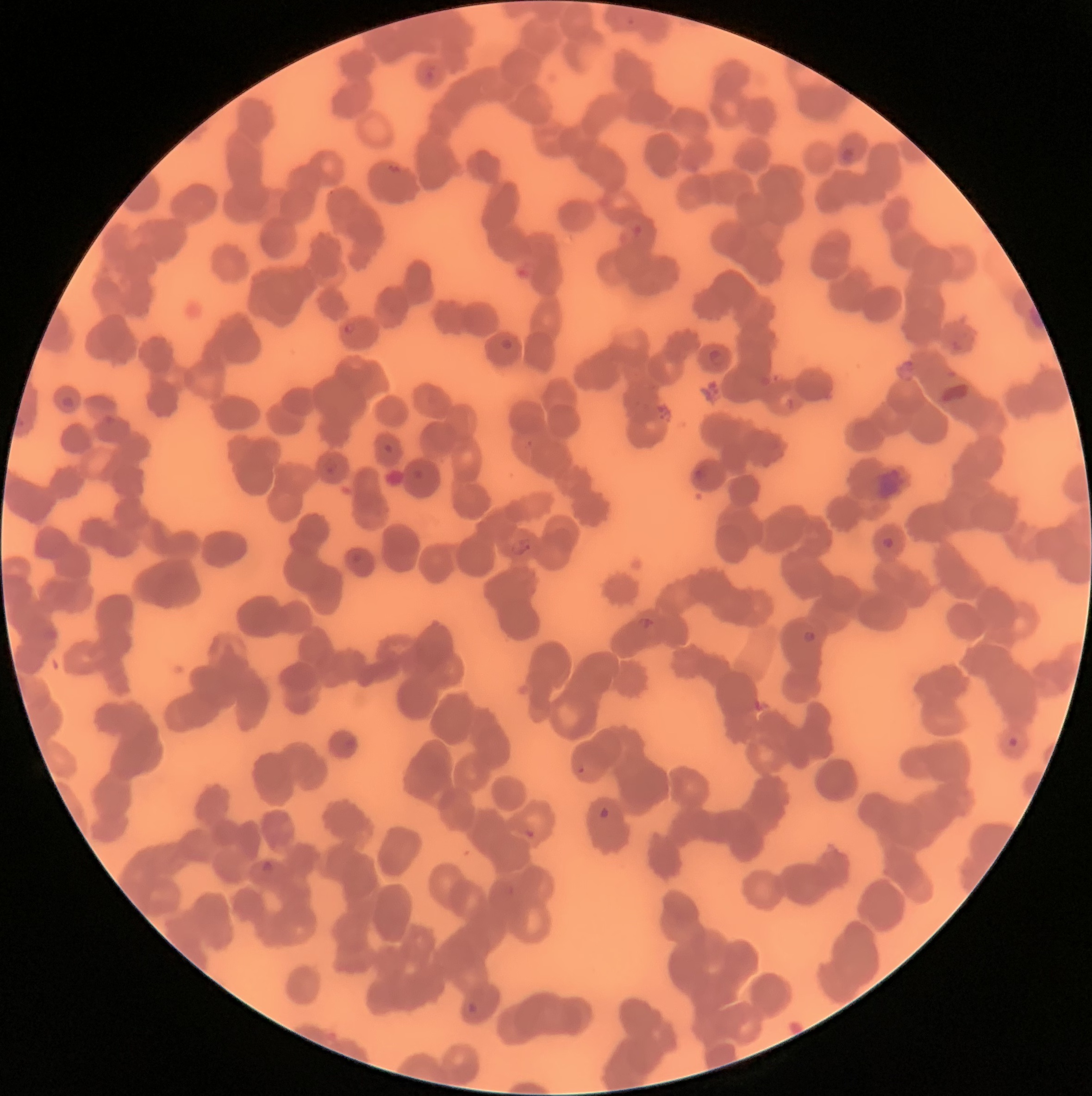
{
  "red_blood_cell_morphology": "rouleaux formation",
  "plasmodium_parasite_locations": "approximate bounding boxes as [x1, y1, x2, y2] in pixels: [626, 17, 635, 26], [422, 65, 436, 83], [840, 147, 856, 166], [341, 322, 357, 335], [501, 338, 513, 351], [708, 347, 727, 368], [61, 395, 74, 408], [323, 457, 340, 475], [880, 536, 895, 550], [508, 538, 534, 558], [637, 616, 654, 630], [802, 630, 816, 644], [1007, 736, 1021, 750], [577, 766, 585, 775], [598, 806, 610, 819], [523, 827, 536, 840], [260, 860, 274, 875], [466, 1001, 479, 1015]",
  "image_size": "1092×1096 pixels",
  "preparation": "thin blood smear",
  "modality": "light microscopy"
}